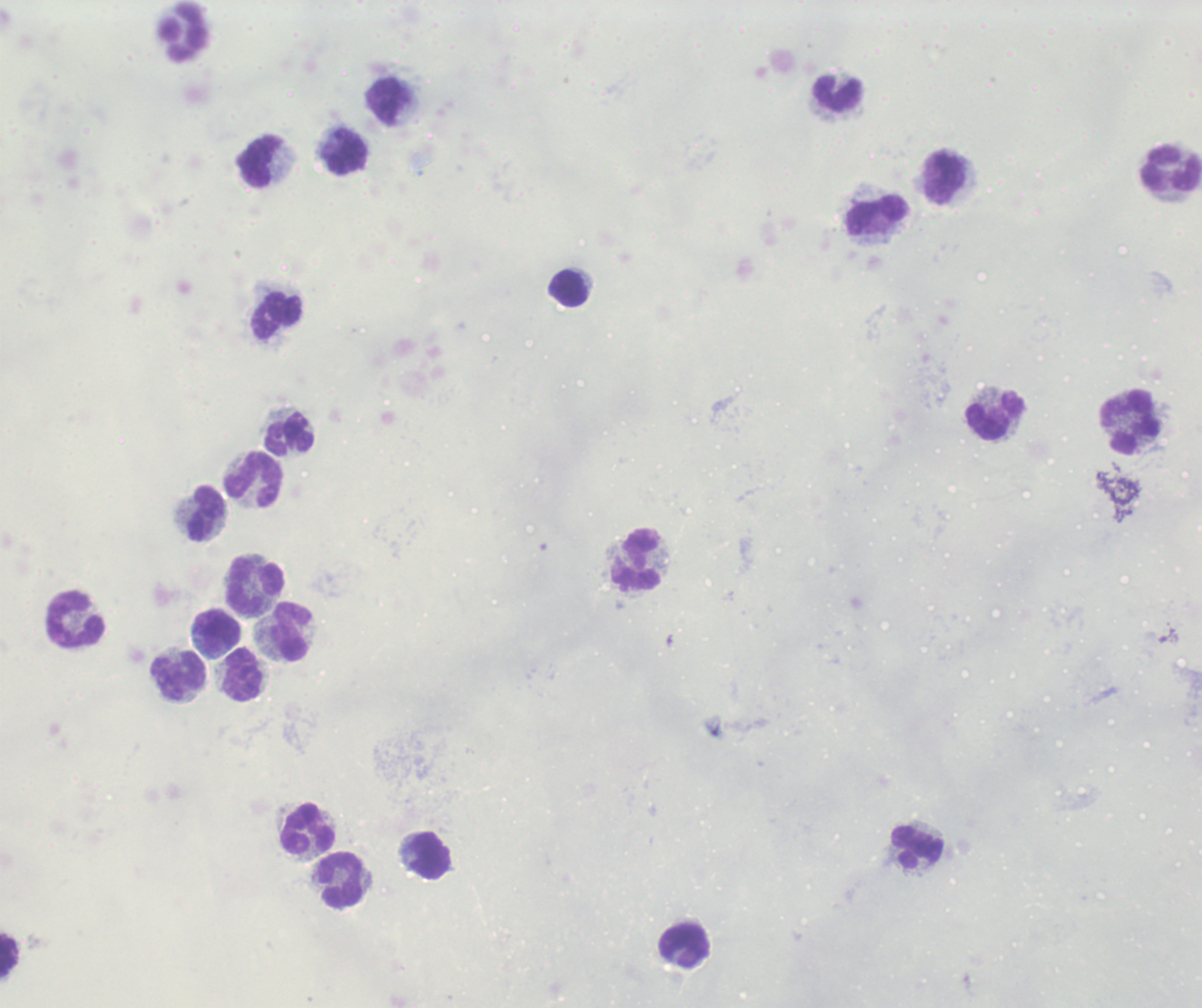
Approximate centers as (x, y) in pixels. Leukocyte locations: (184, 31), (837, 93), (386, 101), (348, 154), (261, 162), (1172, 169), (946, 178), (878, 217), (569, 289), (278, 316), (995, 415), (1130, 422), (290, 434), (254, 480), (209, 514), (635, 560), (256, 587), (77, 619), (217, 626), (292, 633), (178, 675), (244, 676), (308, 829), (919, 848), (431, 855), (341, 879), (685, 946), (9, 956). Thick smear of blood. Image is 1202×1008 pixels. Previously used in an actual diagnosis. Romanowsky stain. Result: negative for malaria parasites. Background quality: unsatisfactory. One field from this slide. 100x magnification.